Describe the morphology of the erythrocytes.
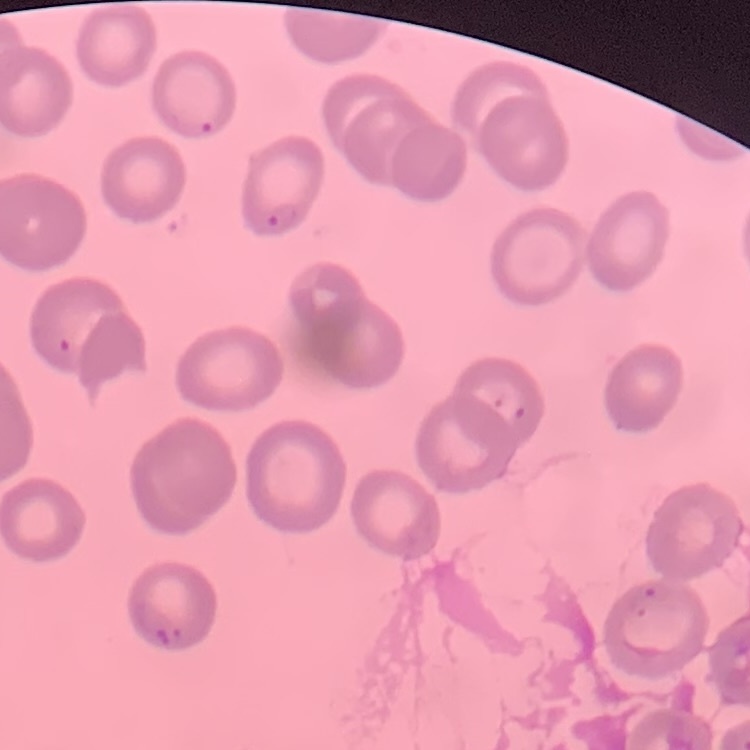

No rouleaux formation.

Square crop of a larger photomicrograph. Thin blood film. Field's or Giemsa stain.